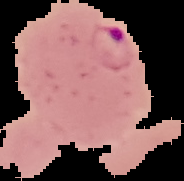

The area outside the segmented cell region is set to black. Image is 184×181 pixels. From a thin blood film. Result: Plasmodium parasites detected.